Identify the blood parasite species.
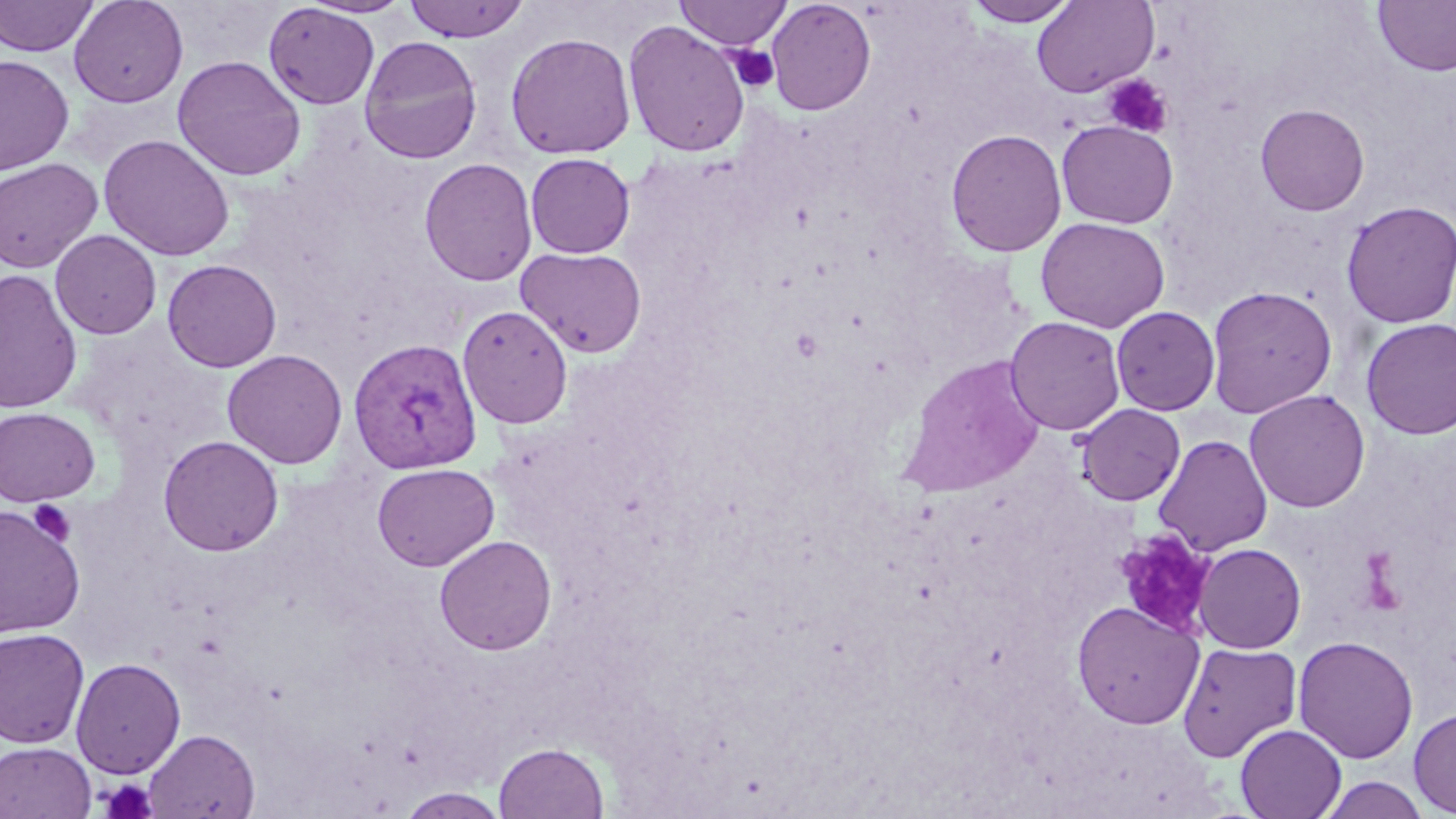
Plasmodium vivax.

Approximate bounding boxes as (x1, y1, x2, y2) in pixels. Platelet locations: (727, 45, 779, 92), (1102, 74, 1174, 138), (28, 499, 77, 546), (1113, 527, 1218, 638), (1359, 548, 1404, 612), (99, 778, 159, 819). Plasmodium vivax-infected red blood cell locations: (348, 337, 482, 473). Uninfected red blood cell locations: (0, 0, 98, 57), (68, 0, 189, 107), (298, 0, 414, 18), (766, 0, 876, 116), (962, 0, 1080, 26), (1031, 0, 1158, 98), (1372, 0, 1456, 76), (402, 1, 529, 42), (674, 1, 793, 50), (263, 3, 380, 109), (622, 20, 750, 158), (505, 32, 636, 159), (358, 36, 482, 164), (0, 55, 74, 175), (172, 55, 306, 181), (1255, 103, 1370, 216), (1056, 120, 1179, 228), (946, 129, 1067, 257), (98, 134, 235, 261), (525, 153, 635, 258), (419, 157, 538, 287), (0, 158, 103, 272), (1340, 200, 1456, 328), (1035, 216, 1170, 333), (50, 230, 161, 339), (515, 246, 647, 358), (162, 259, 282, 372), (0, 267, 83, 415), (1205, 285, 1337, 418), (457, 304, 573, 429), (1110, 306, 1220, 416), (1005, 316, 1126, 435), (1360, 317, 1456, 440), (222, 349, 347, 469), (899, 354, 1047, 496), (1244, 389, 1370, 512), (1076, 403, 1186, 506), (0, 407, 100, 507), (1153, 434, 1274, 556), (158, 435, 284, 556), (372, 462, 499, 571), (0, 501, 87, 640), (434, 534, 557, 655), (1193, 543, 1306, 653), (1071, 600, 1204, 729), (0, 627, 90, 748), (1293, 635, 1418, 764), (1177, 641, 1302, 762), (70, 658, 186, 779), (1408, 706, 1456, 817), (1234, 724, 1346, 819), (143, 729, 259, 819), (0, 741, 96, 819), (493, 741, 609, 819), (1317, 774, 1430, 819), (395, 787, 510, 818). One field of a larger specimen. Image is 1456×819 pixels. Light microscopy. May-Grünwald-Giemsa-stained preparation. Thin blood smear. Captured at 1000x magnification.